Report the malaria status of this cell.
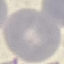
It is uninfected.

Giemsa-stained preparation. Automatically extracted cell patch, resized to 64 × 64 pixels. Acquired by smartphone through the microscope eyepiece. Thin blood film.